Assess this cell for malaria.
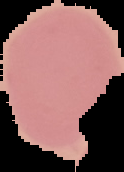

Uninfected.

preparation: thin blood smear
image_type: segmented cell region on a black background
image_size: 124×172 pixels